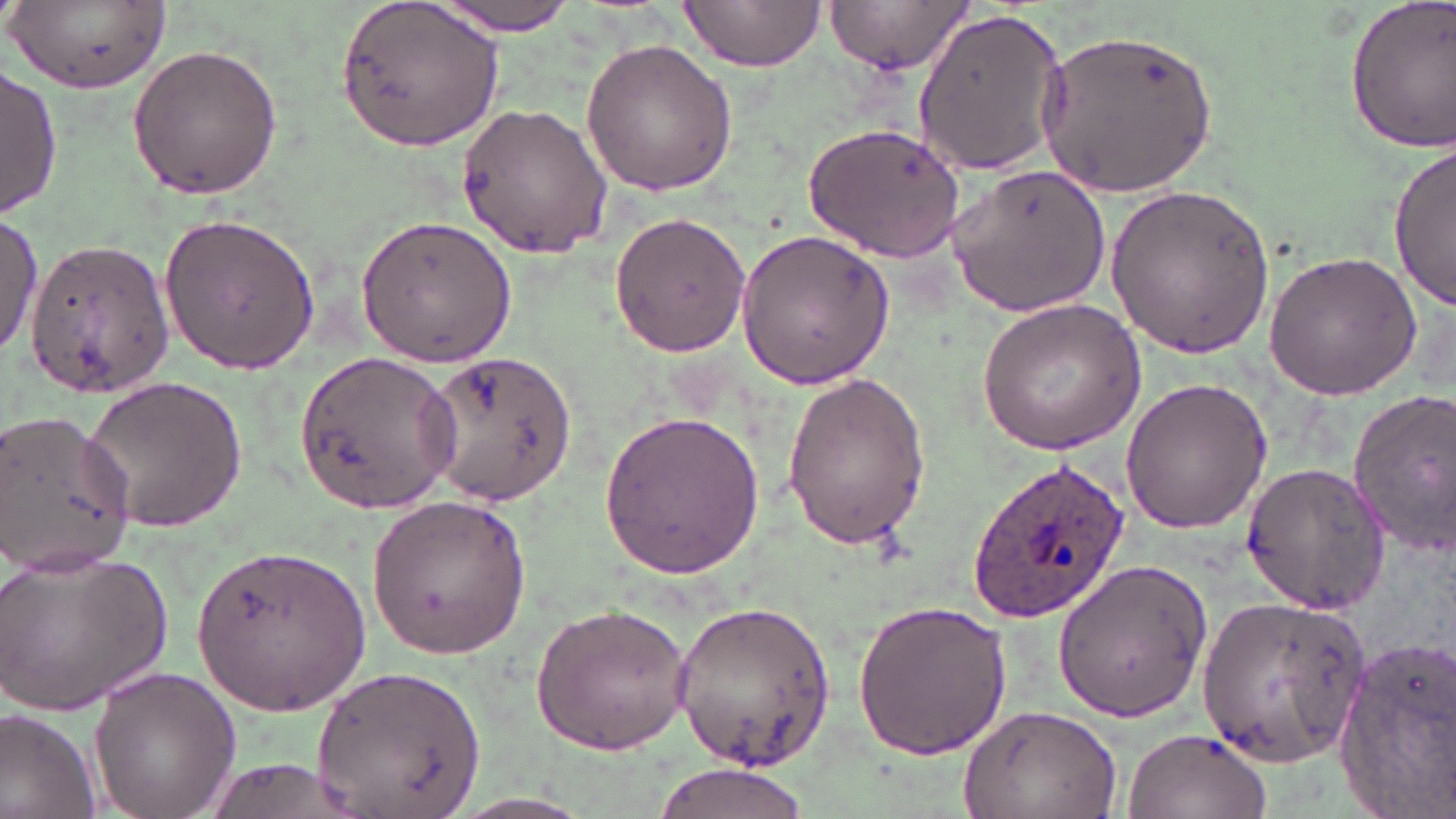

Summary:
  - Coordinate format: approximate bounding boxes as [x1, y1, x2, y2] in pixels
  - Uninfected red blood cell locations: [8, 0, 174, 92], [424, 0, 583, 34], [678, 0, 825, 73], [825, 0, 975, 74], [1343, 0, 1455, 152], [336, 2, 505, 151], [907, 7, 1071, 174], [1043, 27, 1223, 200], [580, 37, 740, 195], [126, 42, 284, 200], [1, 65, 61, 215], [455, 103, 615, 260], [801, 122, 967, 263], [1390, 142, 1455, 308], [945, 163, 1112, 318], [1104, 185, 1280, 356], [609, 209, 752, 359], [159, 212, 323, 374], [354, 213, 521, 368], [0, 214, 41, 356], [735, 230, 895, 389], [23, 236, 177, 403], [1263, 249, 1425, 401], [976, 297, 1146, 457], [294, 349, 462, 512], [426, 349, 578, 506], [779, 370, 931, 552], [79, 373, 249, 533], [1120, 375, 1275, 533], [1343, 389, 1456, 554], [599, 408, 771, 578], [0, 410, 132, 580], [1240, 462, 1389, 616], [365, 491, 532, 661], [192, 541, 371, 713], [0, 542, 173, 716], [1050, 556, 1214, 723], [1195, 593, 1371, 766], [670, 599, 843, 771], [529, 600, 694, 756], [850, 600, 1014, 760], [1328, 639, 1456, 810], [86, 664, 241, 819], [310, 666, 486, 819], [959, 701, 1125, 819], [0, 707, 99, 819], [1121, 728, 1273, 819], [647, 764, 820, 819]
  - Plasmodium ovale-infected red blood cell locations: [964, 460, 1133, 626]
  - Slide-level diagnosis: Plasmodium ovale
  - Preparation: thin blood film
  - Image size: 1456×819 pixels
  - Stain: May-Grünwald-Giemsa
  - Modality: optical microscopy
  - Field of view: single
  - Magnification: 1000x